Name the parasite shown.
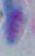

Toxoplasma gondii.

Summary:
  - Modality: photomicrograph
  - Magnification: 1000x